Assess this cell for malaria.
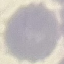
Uninfected.

Giemsa-stained preparation. Thin smear of blood. Cell patch, automatically extracted from a larger field of view and resized to 64 × 64 pixels. Acquired by smartphone through the microscope eyepiece.